Name the parasite shown.
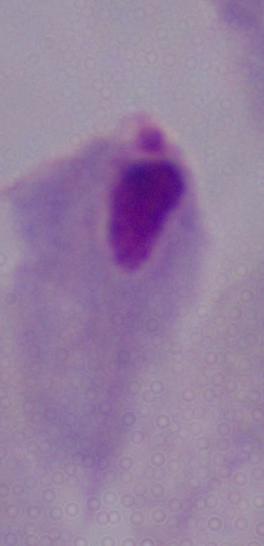
This is a trichomonad.

Summary:
  - Modality: micrograph
  - Magnification: 1000x